Assess this cell for malaria.
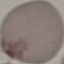
It is uninfected.

preparation = thin blood film
stain = Giemsa
image type = automatically extracted cell patch, resized to 64 × 64 pixels
capture = smartphone through the microscope eyepiece